Name the blood parasite species.
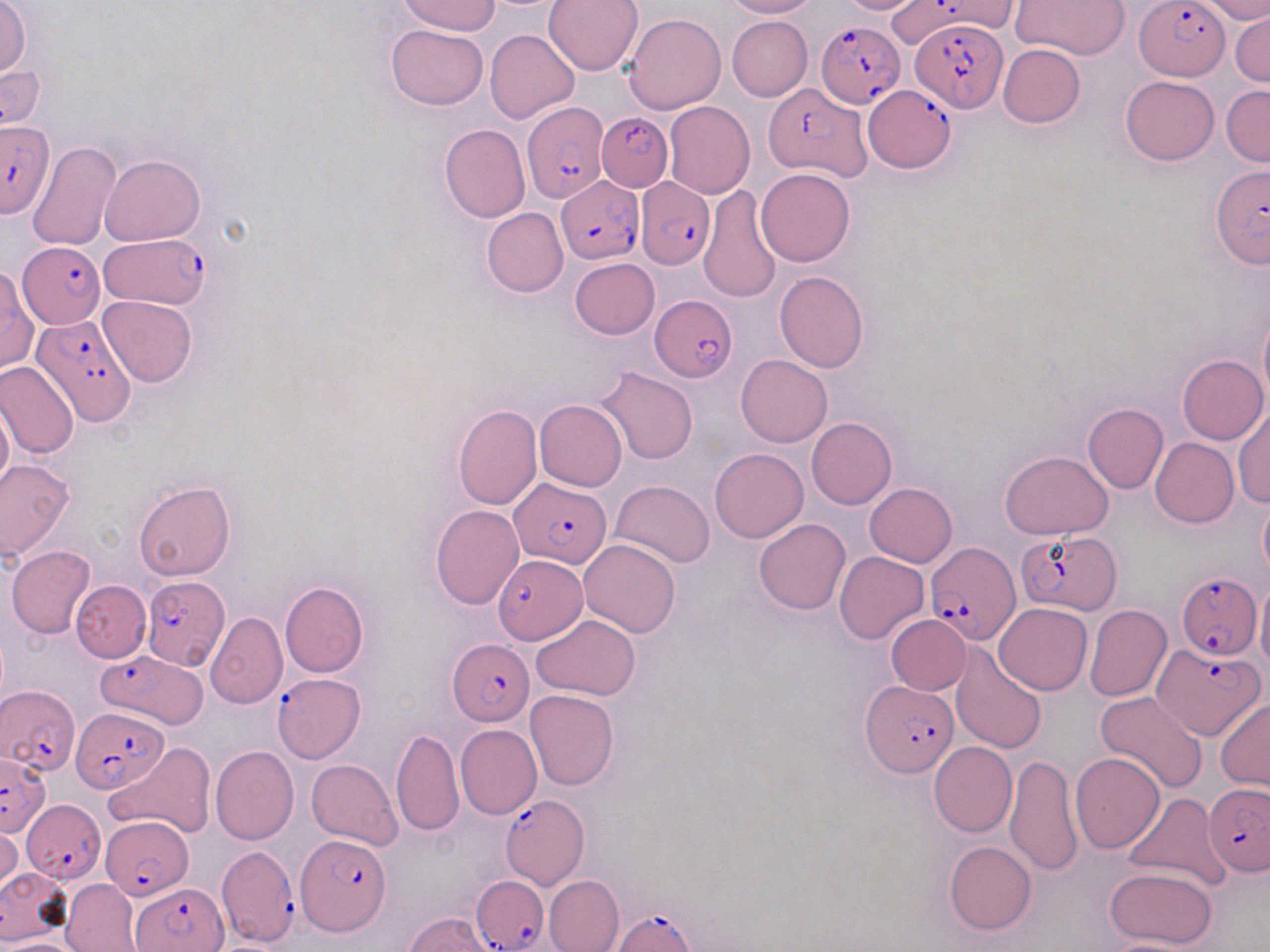
Plasmodium falciparum.

Summary:
  - Coordinate format: approximate bounding boxes as (x1, y1, x2, y2) in pixels
  - Plasmodium falciparum-infected red blood cell locations: (1134, 0, 1231, 80), (885, 2, 975, 52), (816, 19, 905, 108), (910, 19, 1008, 113), (762, 82, 871, 180), (866, 86, 955, 173), (522, 102, 609, 204), (598, 112, 672, 191), (0, 122, 54, 218), (1210, 162, 1268, 268), (558, 176, 643, 263), (635, 179, 713, 271), (98, 233, 210, 310), (20, 243, 107, 326), (650, 296, 736, 380), (27, 313, 134, 429), (510, 479, 612, 568), (1016, 528, 1123, 614), (925, 541, 1017, 646), (487, 559, 591, 647), (1175, 570, 1261, 662), (140, 576, 230, 670), (448, 640, 534, 725), (1153, 641, 1263, 740), (96, 650, 209, 729), (271, 674, 364, 763), (860, 679, 957, 777), (0, 682, 80, 778), (75, 706, 167, 793), (0, 754, 49, 834), (1203, 783, 1270, 877), (501, 793, 589, 891), (21, 801, 105, 884), (101, 816, 192, 899), (293, 833, 390, 934), (216, 845, 302, 946), (471, 876, 548, 952), (131, 881, 229, 951), (614, 907, 698, 950)
  - Uninfected red blood cell locations: (0, 0, 31, 78), (396, 0, 501, 35), (545, 0, 643, 75), (722, 0, 817, 19), (836, 0, 926, 15), (1014, 0, 1130, 59), (1200, 1, 1270, 23), (1230, 10, 1270, 88), (623, 13, 727, 114), (726, 16, 813, 101), (386, 24, 488, 111), (485, 28, 579, 123), (997, 44, 1085, 128), (1, 49, 45, 135), (1120, 75, 1219, 165), (1220, 85, 1270, 165), (663, 101, 755, 199), (440, 123, 529, 223), (26, 140, 121, 250), (100, 155, 205, 244), (756, 167, 855, 266), (698, 187, 781, 304), (482, 208, 569, 297), (569, 258, 660, 339), (1, 263, 38, 376), (774, 270, 869, 373), (98, 296, 198, 387), (1258, 311, 1270, 413), (1176, 354, 1268, 445), (737, 355, 832, 447), (0, 359, 78, 459), (596, 366, 698, 465), (1, 396, 13, 497), (535, 399, 627, 491), (1083, 402, 1168, 494), (452, 404, 541, 510), (1232, 406, 1269, 508), (806, 418, 897, 510), (1150, 437, 1239, 527), (710, 448, 808, 543), (1000, 451, 1114, 540), (0, 458, 75, 560), (610, 480, 715, 567), (133, 481, 235, 582), (864, 482, 957, 567), (1258, 492, 1270, 586), (430, 505, 524, 609), (753, 519, 852, 615), (578, 539, 681, 639), (6, 545, 96, 638), (833, 550, 929, 644), (1255, 571, 1270, 677), (71, 581, 151, 662), (279, 582, 369, 678), (993, 603, 1092, 694), (1084, 604, 1171, 702), (206, 611, 287, 708), (886, 614, 971, 694), (532, 616, 640, 700), (950, 642, 1046, 753), (525, 690, 619, 790), (1095, 690, 1207, 794), (1216, 697, 1270, 792), (456, 723, 542, 820), (390, 729, 464, 838), (929, 741, 1017, 837), (104, 742, 215, 840), (210, 745, 298, 844), (1071, 752, 1164, 853), (1005, 754, 1084, 876), (307, 758, 402, 850), (1122, 793, 1230, 889), (1, 823, 22, 896), (943, 841, 1036, 936), (0, 864, 71, 943), (1103, 865, 1218, 949), (543, 875, 624, 952), (61, 879, 141, 951), (406, 912, 497, 952), (1096, 938, 1201, 952), (6, 939, 77, 952)
  - Stain: May-Grünwald-Giemsa
  - Field of view: one of a larger specimen
  - Image size: 1270×952 pixels
  - Magnification: 1000x
  - Preparation: thin blood film
  - Modality: optical microscopy